Report the malaria status of this cell.
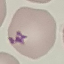

Uninfected.

Summary:
  - Stain: Giemsa
  - Preparation: thin blood film
  - Capture: smartphone through the microscope eyepiece
  - Image type: automatically extracted cell patch, resized to 64 × 64 pixels